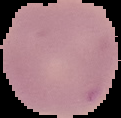

{
  "image_type": "segmented cell region with the area outside set to black",
  "malaria_status": "uninfected",
  "preparation": "thin blood smear",
  "image_size": "121×118 pixels"
}